Report the malaria status of this cell.
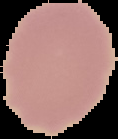

Uninfected.

From a thin blood film. Image is 118×139 pixels. The area outside the segmented cell region is set to black.